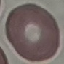 Malaria status: uninfected. Acquired by smartphone through the microscope eyepiece. Cell patch, automatically extracted from a larger field of view and resized to 64 × 64 pixels. Giemsa-stained preparation. Thin blood smear.